Give the position of every malaria parasite.
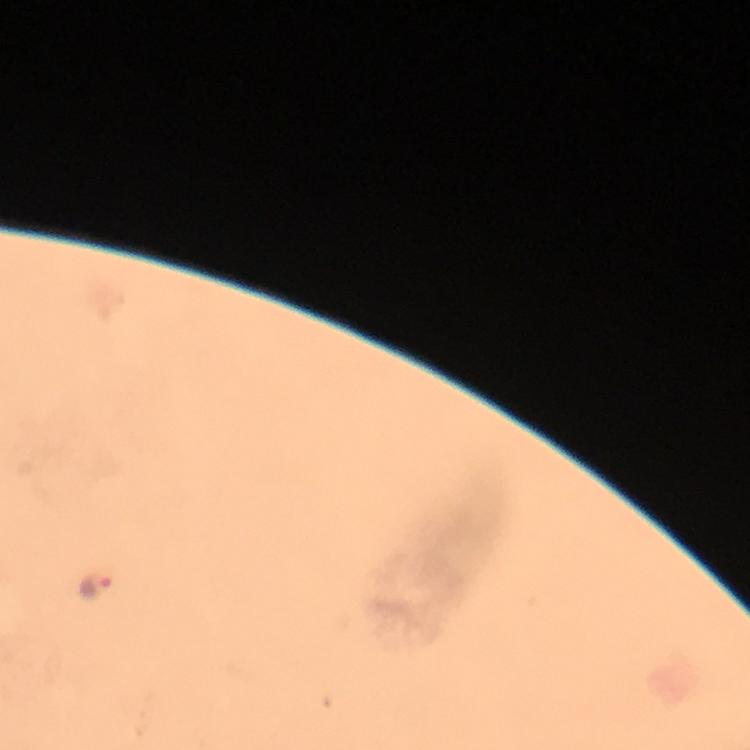
Approximate centers as {x, y} in pixels.
Malaria parasites: {94, 586}.

stain = Giemsa
image size = 750×750 pixels
magnification = 100x
preparation = thick blood film
context = from a diagnostic examination for malaria
immersion oil = applied
cropped from = one field of view
capture = smartphone camera through the microscope